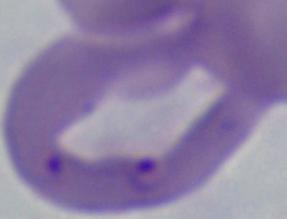

{
  "magnification": "1000x",
  "modality": "photomicrograph",
  "identification": "Babesia"
}